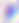

modality = photomicrograph
magnification = 400x
identification = Toxoplasma gondii